Identify the blood parasite species.
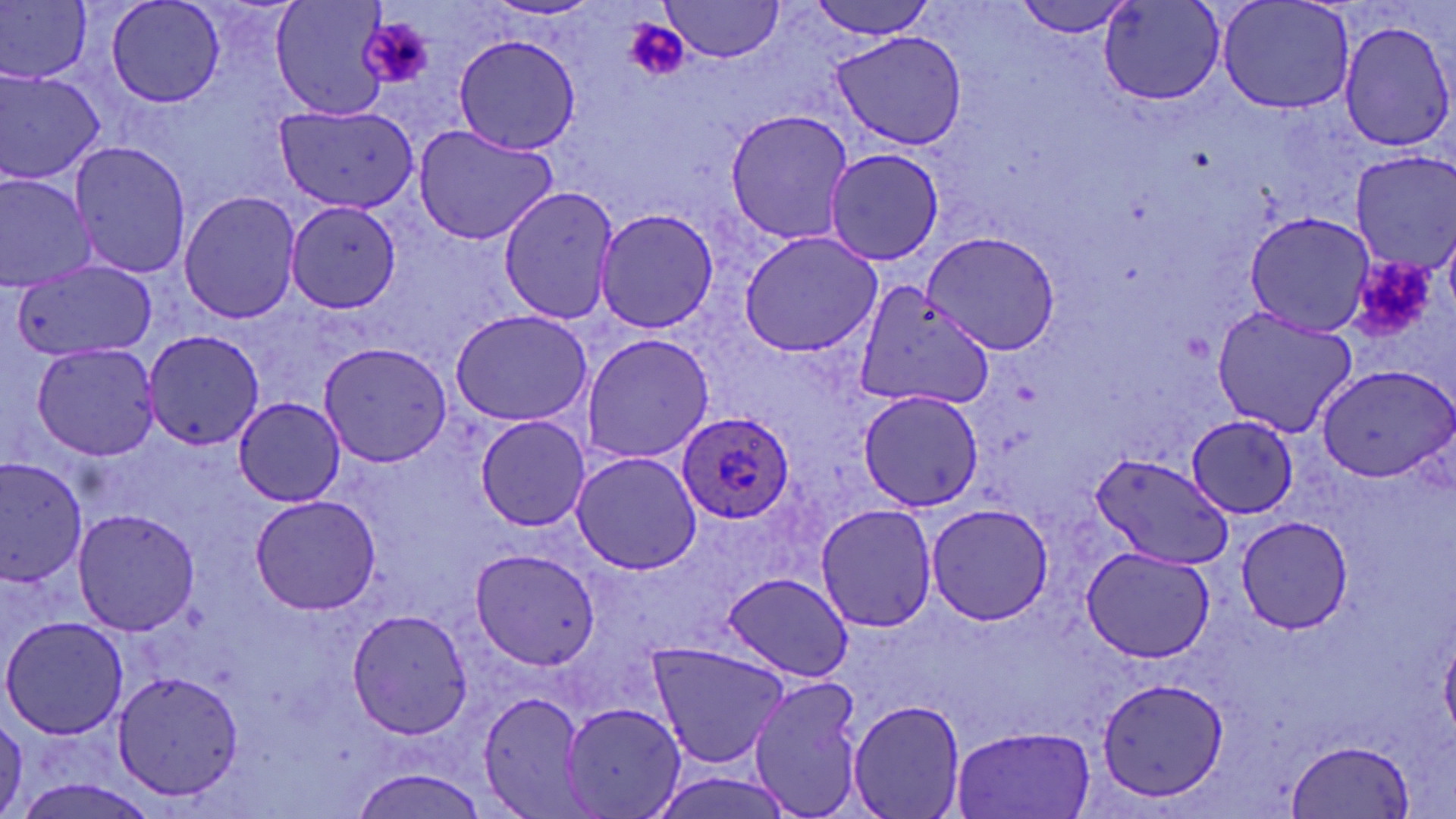
Plasmodium ovale.

Approximate bounding boxes as named x1/y1/x2/y2 corners in pixels. Plasmodium ovale-infected red blood cell locations: (x1=678, y1=415, x2=797, y2=523). Uninfected red blood cell locations: (x1=103, y1=0, x2=227, y2=107), (x1=269, y1=0, x2=396, y2=120), (x1=661, y1=0, x2=787, y2=63), (x1=803, y1=0, x2=940, y2=37), (x1=1011, y1=0, x2=1138, y2=37), (x1=0, y1=1, x2=95, y2=86), (x1=1099, y1=1, x2=1227, y2=107), (x1=1217, y1=1, x2=1354, y2=112), (x1=1337, y1=19, x2=1456, y2=153), (x1=831, y1=31, x2=966, y2=151), (x1=452, y1=34, x2=583, y2=154), (x1=0, y1=67, x2=108, y2=187), (x1=274, y1=104, x2=421, y2=214), (x1=723, y1=109, x2=853, y2=245), (x1=411, y1=125, x2=560, y2=245), (x1=69, y1=139, x2=192, y2=281), (x1=824, y1=147, x2=947, y2=266), (x1=1345, y1=152, x2=1456, y2=274), (x1=0, y1=170, x2=99, y2=294), (x1=498, y1=185, x2=622, y2=323), (x1=178, y1=189, x2=302, y2=323), (x1=285, y1=199, x2=405, y2=317), (x1=593, y1=205, x2=721, y2=336), (x1=1244, y1=211, x2=1376, y2=338), (x1=919, y1=228, x2=1063, y2=355), (x1=737, y1=229, x2=883, y2=358), (x1=10, y1=258, x2=155, y2=362), (x1=855, y1=281, x2=994, y2=411), (x1=1211, y1=306, x2=1360, y2=436), (x1=448, y1=307, x2=592, y2=425), (x1=141, y1=328, x2=264, y2=450), (x1=580, y1=332, x2=714, y2=464), (x1=317, y1=340, x2=454, y2=468), (x1=29, y1=341, x2=162, y2=462), (x1=1316, y1=365, x2=1454, y2=484), (x1=857, y1=388, x2=987, y2=511), (x1=233, y1=397, x2=347, y2=506), (x1=474, y1=414, x2=590, y2=531), (x1=1187, y1=416, x2=1299, y2=518), (x1=1088, y1=450, x2=1234, y2=569), (x1=570, y1=451, x2=702, y2=573), (x1=0, y1=459, x2=88, y2=588), (x1=247, y1=495, x2=379, y2=615), (x1=814, y1=501, x2=939, y2=634), (x1=922, y1=503, x2=1055, y2=626), (x1=72, y1=506, x2=198, y2=638), (x1=1233, y1=517, x2=1357, y2=636), (x1=1080, y1=543, x2=1217, y2=662), (x1=468, y1=548, x2=598, y2=672), (x1=722, y1=572, x2=852, y2=681), (x1=346, y1=606, x2=475, y2=739), (x1=1, y1=614, x2=128, y2=742), (x1=645, y1=638, x2=793, y2=770), (x1=112, y1=669, x2=248, y2=802), (x1=748, y1=674, x2=868, y2=817), (x1=1095, y1=675, x2=1231, y2=806), (x1=476, y1=690, x2=590, y2=816), (x1=847, y1=699, x2=966, y2=819), (x1=563, y1=701, x2=687, y2=817), (x1=0, y1=713, x2=31, y2=812), (x1=950, y1=726, x2=1096, y2=817), (x1=1287, y1=740, x2=1415, y2=817), (x1=349, y1=767, x2=492, y2=817), (x1=16, y1=782, x2=158, y2=819). Platelet locations: (x1=359, y1=18, x2=436, y2=90), (x1=624, y1=18, x2=685, y2=77), (x1=1352, y1=258, x2=1437, y2=342). Captured at 1000x magnification. Image is 1456×819 pixels. Optical microscopy. One field of a larger specimen. May-Grünwald-Giemsa stain. Thin blood smear.